Assess this cell for malaria.
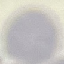
It is uninfected.

image_type: automatically extracted cell patch, resized to 64 × 64 pixels
capture: smartphone through the microscope eyepiece
preparation: thin blood smear
stain: Giemsa